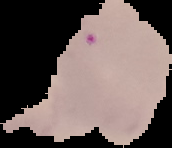

image_type: segmented cell region with the area outside set to black
image_size: 172×148 pixels
result: malaria parasites identified
preparation: thin blood film